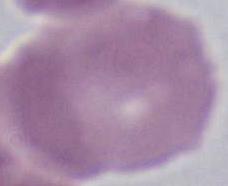
{
  "magnification": "1000x",
  "identification": "erythrocyte",
  "modality": "photomicrograph"
}